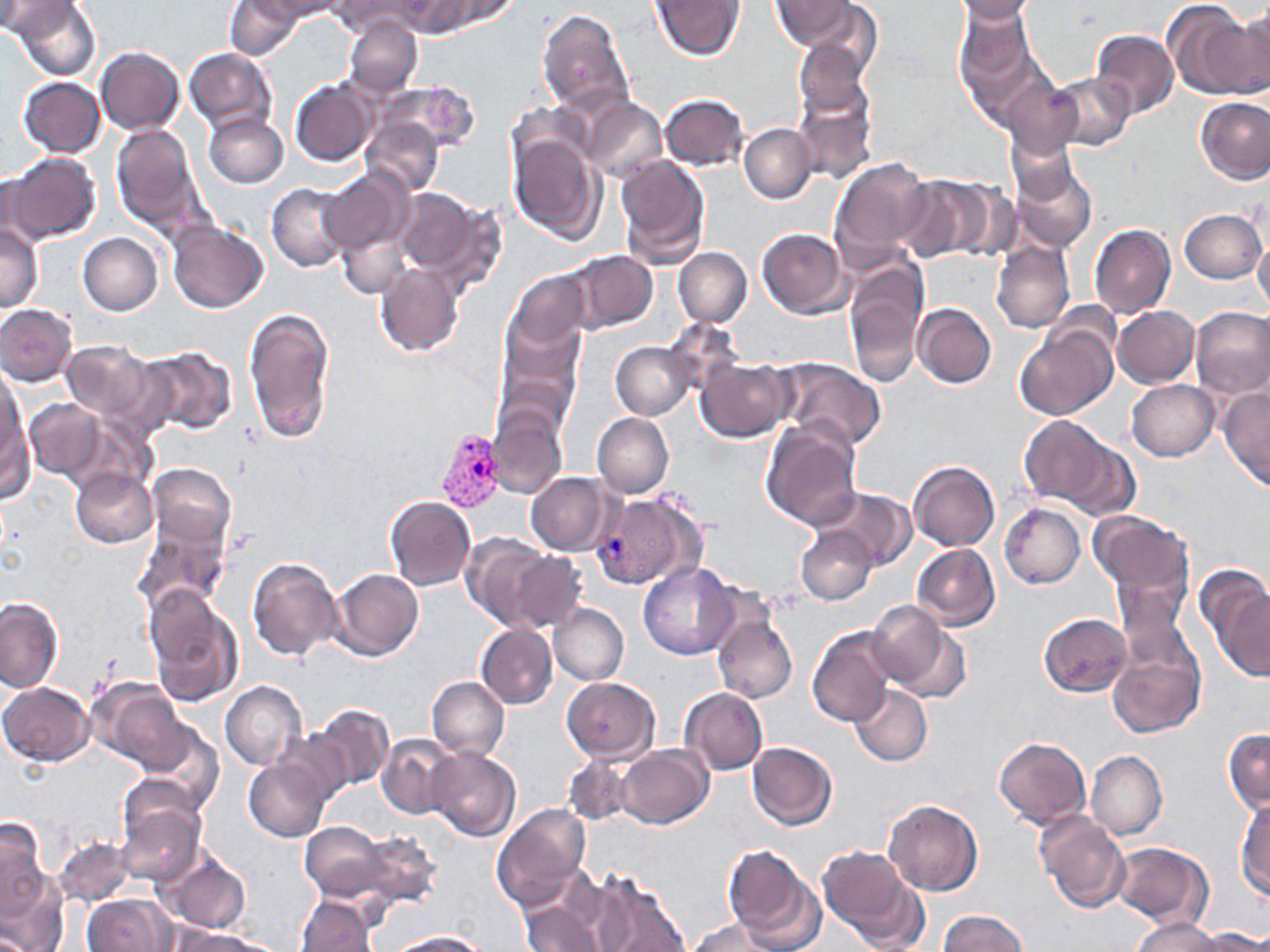 Approximate bounding boxes as named x1/y1/x2/y2 corners in pixels. Plasmodium vivax-infected red blood cell locations: (x1=437, y1=429, x2=505, y2=512), (x1=593, y1=490, x2=705, y2=590). Uninfected red blood cell locations: (x1=12, y1=0, x2=102, y2=80), (x1=224, y1=0, x2=302, y2=60), (x1=261, y1=0, x2=347, y2=20), (x1=331, y1=0, x2=429, y2=36), (x1=408, y1=0, x2=511, y2=36), (x1=652, y1=0, x2=743, y2=60), (x1=772, y1=0, x2=856, y2=50), (x1=948, y1=0, x2=1040, y2=22), (x1=0, y1=2, x2=77, y2=38), (x1=1165, y1=2, x2=1265, y2=99), (x1=798, y1=3, x2=883, y2=82), (x1=1228, y1=3, x2=1270, y2=96), (x1=955, y1=6, x2=1037, y2=102), (x1=537, y1=9, x2=634, y2=116), (x1=345, y1=16, x2=422, y2=95), (x1=1090, y1=29, x2=1178, y2=118), (x1=795, y1=38, x2=874, y2=117), (x1=95, y1=47, x2=183, y2=135), (x1=184, y1=49, x2=275, y2=131), (x1=1050, y1=73, x2=1134, y2=150), (x1=18, y1=77, x2=105, y2=157), (x1=1002, y1=79, x2=1082, y2=158), (x1=291, y1=80, x2=376, y2=166), (x1=381, y1=81, x2=481, y2=155), (x1=793, y1=89, x2=877, y2=185), (x1=660, y1=93, x2=749, y2=170), (x1=1195, y1=96, x2=1270, y2=184), (x1=581, y1=97, x2=666, y2=183), (x1=203, y1=113, x2=288, y2=188), (x1=362, y1=117, x2=444, y2=196), (x1=739, y1=123, x2=815, y2=203), (x1=112, y1=124, x2=207, y2=237), (x1=1007, y1=131, x2=1078, y2=205), (x1=509, y1=132, x2=603, y2=243), (x1=5, y1=152, x2=100, y2=243), (x1=615, y1=154, x2=710, y2=267), (x1=831, y1=156, x2=935, y2=258), (x1=1011, y1=158, x2=1097, y2=251), (x1=320, y1=167, x2=412, y2=254), (x1=0, y1=171, x2=47, y2=251), (x1=897, y1=175, x2=988, y2=262), (x1=943, y1=181, x2=1022, y2=261), (x1=266, y1=183, x2=353, y2=273), (x1=395, y1=189, x2=493, y2=284), (x1=1179, y1=209, x2=1267, y2=284), (x1=167, y1=219, x2=268, y2=313), (x1=335, y1=223, x2=410, y2=299), (x1=0, y1=224, x2=43, y2=312), (x1=1089, y1=225, x2=1175, y2=320), (x1=757, y1=228, x2=846, y2=318), (x1=1253, y1=232, x2=1270, y2=317), (x1=78, y1=233, x2=163, y2=315), (x1=991, y1=240, x2=1074, y2=334), (x1=673, y1=247, x2=752, y2=327), (x1=565, y1=250, x2=658, y2=333), (x1=374, y1=263, x2=465, y2=357), (x1=844, y1=269, x2=926, y2=389), (x1=506, y1=271, x2=589, y2=349), (x1=915, y1=303, x2=996, y2=388), (x1=0, y1=305, x2=77, y2=385), (x1=244, y1=305, x2=337, y2=445), (x1=1112, y1=306, x2=1199, y2=388), (x1=1190, y1=307, x2=1270, y2=399), (x1=501, y1=315, x2=582, y2=414), (x1=1016, y1=323, x2=1118, y2=422), (x1=59, y1=338, x2=162, y2=426), (x1=611, y1=341, x2=693, y2=419), (x1=135, y1=346, x2=238, y2=435), (x1=696, y1=358, x2=794, y2=441), (x1=778, y1=359, x2=887, y2=451), (x1=0, y1=367, x2=27, y2=468), (x1=1126, y1=380, x2=1219, y2=461), (x1=1218, y1=387, x2=1270, y2=491), (x1=24, y1=400, x2=106, y2=481), (x1=486, y1=408, x2=567, y2=500), (x1=2, y1=412, x2=36, y2=505), (x1=591, y1=413, x2=674, y2=498), (x1=1019, y1=415, x2=1112, y2=507), (x1=762, y1=420, x2=861, y2=531), (x1=1060, y1=438, x2=1141, y2=520), (x1=909, y1=461, x2=1000, y2=551), (x1=147, y1=464, x2=236, y2=548), (x1=71, y1=467, x2=157, y2=548), (x1=527, y1=472, x2=615, y2=555), (x1=817, y1=487, x2=915, y2=570), (x1=384, y1=496, x2=477, y2=590), (x1=1000, y1=504, x2=1085, y2=588), (x1=1090, y1=510, x2=1192, y2=599), (x1=136, y1=517, x2=229, y2=614), (x1=796, y1=527, x2=875, y2=605), (x1=461, y1=533, x2=557, y2=629), (x1=912, y1=544, x2=999, y2=630), (x1=503, y1=549, x2=587, y2=633), (x1=247, y1=556, x2=342, y2=661), (x1=638, y1=563, x2=737, y2=659), (x1=1198, y1=568, x2=1270, y2=679), (x1=331, y1=569, x2=422, y2=661), (x1=1112, y1=571, x2=1193, y2=675), (x1=144, y1=587, x2=243, y2=706), (x1=1, y1=597, x2=64, y2=693), (x1=866, y1=599, x2=970, y2=703), (x1=548, y1=603, x2=628, y2=685), (x1=711, y1=612, x2=798, y2=703), (x1=1039, y1=613, x2=1131, y2=696), (x1=476, y1=624, x2=557, y2=710), (x1=808, y1=626, x2=898, y2=728), (x1=1108, y1=649, x2=1202, y2=739), (x1=427, y1=676, x2=508, y2=761), (x1=562, y1=678, x2=660, y2=763), (x1=220, y1=681, x2=305, y2=770), (x1=0, y1=682, x2=94, y2=765), (x1=849, y1=684, x2=932, y2=767), (x1=100, y1=686, x2=194, y2=773), (x1=679, y1=688, x2=767, y2=776), (x1=307, y1=704, x2=394, y2=792), (x1=140, y1=727, x2=225, y2=817), (x1=1224, y1=728, x2=1269, y2=815), (x1=274, y1=731, x2=351, y2=806), (x1=377, y1=732, x2=457, y2=819), (x1=994, y1=737, x2=1089, y2=829), (x1=746, y1=742, x2=836, y2=830), (x1=614, y1=745, x2=713, y2=830), (x1=428, y1=748, x2=520, y2=842), (x1=1086, y1=751, x2=1166, y2=841), (x1=563, y1=755, x2=629, y2=825), (x1=244, y1=758, x2=332, y2=842), (x1=1235, y1=797, x2=1270, y2=897), (x1=883, y1=799, x2=982, y2=897), (x1=115, y1=802, x2=203, y2=886), (x1=492, y1=805, x2=591, y2=911), (x1=1036, y1=811, x2=1131, y2=915), (x1=0, y1=818, x2=50, y2=912), (x1=300, y1=821, x2=392, y2=900), (x1=355, y1=828, x2=441, y2=906), (x1=54, y1=837, x2=133, y2=908), (x1=1110, y1=843, x2=1213, y2=929), (x1=722, y1=847, x2=821, y2=951), (x1=818, y1=847, x2=920, y2=946), (x1=158, y1=851, x2=250, y2=933), (x1=0, y1=870, x2=66, y2=951), (x1=591, y1=878, x2=691, y2=952), (x1=83, y1=893, x2=175, y2=952), (x1=297, y1=895, x2=378, y2=952), (x1=520, y1=895, x2=606, y2=952), (x1=938, y1=909, x2=1027, y2=951), (x1=1132, y1=917, x2=1222, y2=951), (x1=689, y1=918, x2=784, y2=952), (x1=1197, y1=928, x2=1270, y2=951), (x1=179, y1=929, x2=275, y2=952), (x1=387, y1=931, x2=488, y2=951). Slide-level diagnosis: Plasmodium vivax. Light microscopy. Thin blood film. Image is 1270×952 pixels. One field of a larger specimen. May-Grünwald-Giemsa-stained preparation. 1000x magnification.